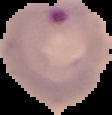
Summary:
  - Image type: segmented cell region on a black background
  - Result: Plasmodium parasites detected
  - Image size: 112×115 pixels
  - Preparation: thin blood film